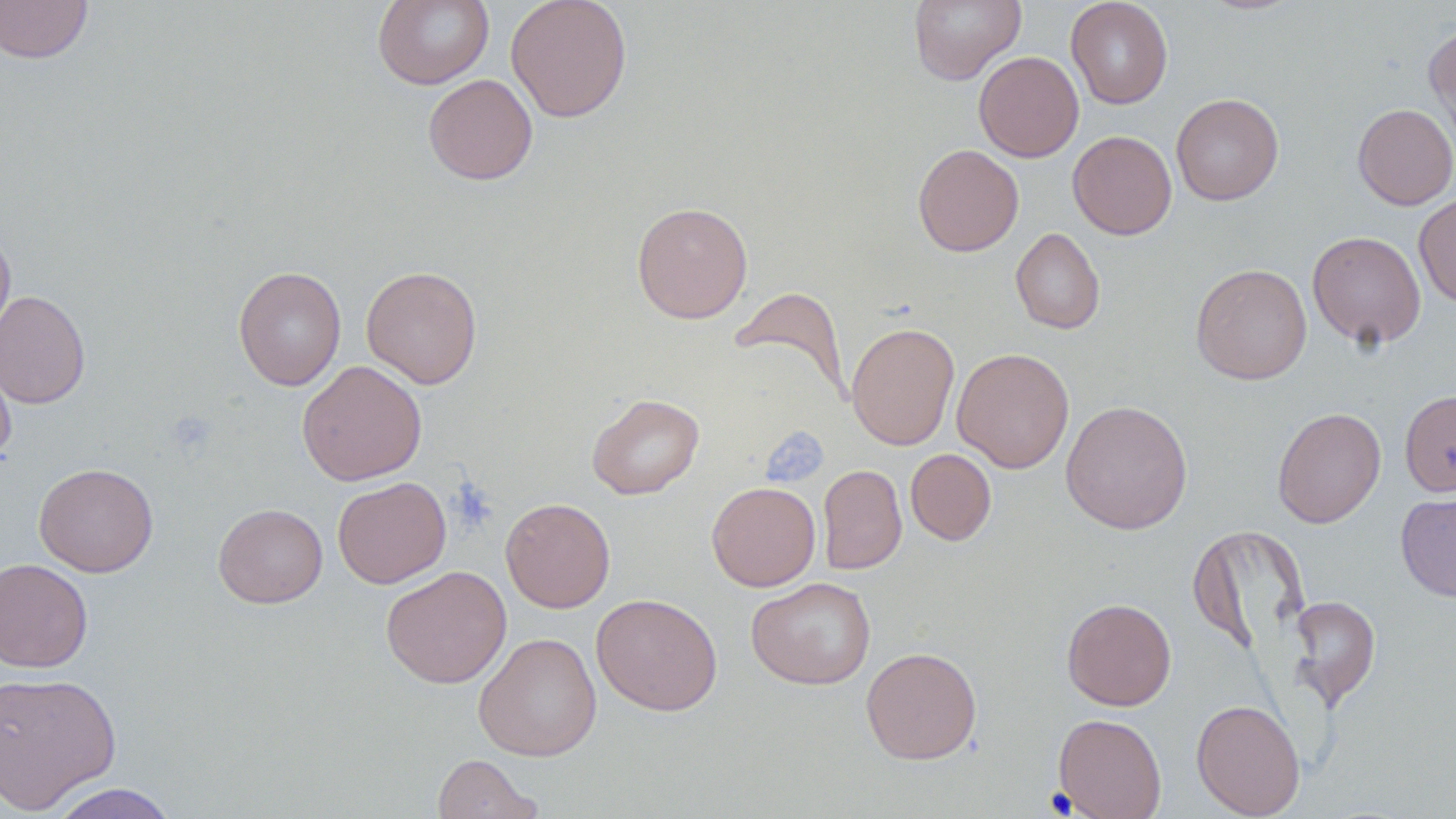

Summary:
  - Coordinate format: approximate bounding boxes as (x1, y1, x2, y2) in pixels
  - Uninfected red blood cell locations: (0, 0, 93, 64), (372, 0, 494, 89), (505, 0, 633, 122), (908, 0, 1025, 85), (1065, 0, 1173, 109), (1424, 22, 1456, 148), (973, 51, 1084, 162), (423, 74, 538, 185), (1171, 93, 1284, 206), (1353, 103, 1456, 210), (1068, 131, 1177, 240), (913, 143, 1024, 257), (1414, 193, 1456, 307), (632, 202, 753, 324), (0, 226, 15, 346), (1011, 228, 1105, 334), (1307, 231, 1426, 350), (1190, 263, 1312, 385), (233, 265, 346, 390), (361, 265, 483, 389), (729, 285, 851, 400), (0, 289, 91, 409), (846, 321, 960, 451), (0, 345, 16, 465), (951, 348, 1075, 473), (297, 360, 427, 486), (1400, 389, 1456, 496), (587, 393, 704, 499), (1061, 400, 1193, 534), (1271, 406, 1386, 528), (905, 449, 996, 546), (33, 462, 159, 577), (818, 464, 907, 575), (332, 476, 451, 589), (706, 481, 821, 591), (1396, 490, 1456, 602), (500, 497, 615, 613), (213, 503, 328, 608), (1187, 524, 1310, 656), (0, 557, 93, 672), (380, 565, 511, 688), (746, 577, 876, 690), (592, 592, 722, 715), (1287, 595, 1381, 710), (1062, 597, 1176, 711), (473, 631, 602, 761), (861, 646, 982, 765), (0, 671, 122, 813), (1191, 698, 1306, 818), (1053, 713, 1167, 819), (432, 754, 543, 819), (47, 783, 179, 819)
  - Slide-level diagnosis: no evidence of blood parasites
  - Preparation: thin blood film
  - Stain: May-Grünwald-Giemsa
  - Image size: 1456×819 pixels
  - Magnification: 1000x
  - Modality: optical microscopy
  - Field of view: single